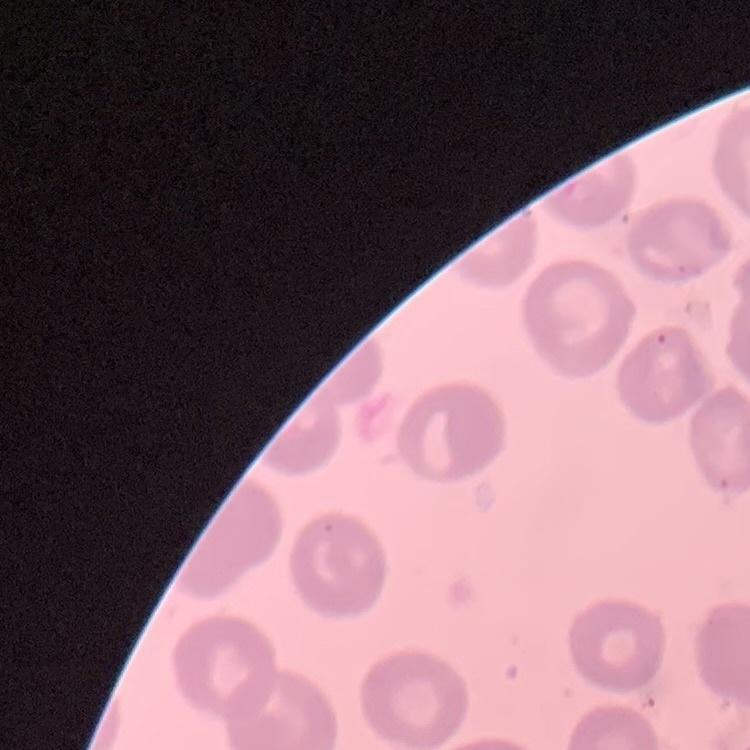 The erythrocytes exhibit no rouleaux formation. Square crop of a larger photomicrograph. Thin blood smear. Stained with either Field's or Giemsa.